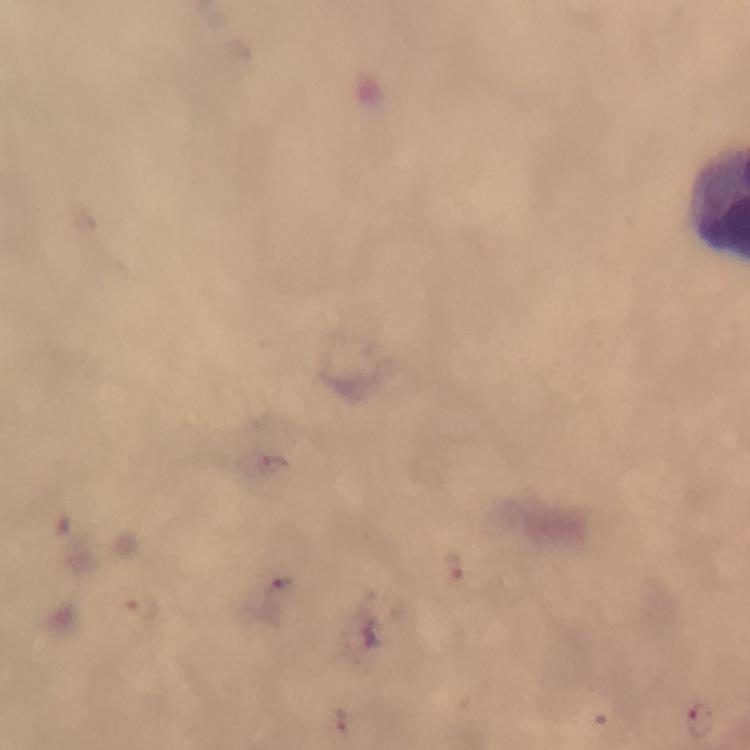
magnification = 100x
immersion oil = applied
stain = Giemsa
context = from a malaria diagnostic workup
image size = 750×750 pixels
preparation = thick blood smear
cropped from = one field of view
Plasmodium parasite locations = approximate centers as (x, y) in pixels: (268, 464), (454, 568), (284, 590), (139, 608), (340, 720), (699, 721)
capture = smartphone mounted on the microscope